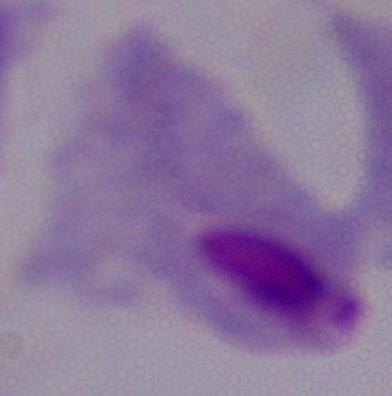
magnification = 1000x
modality = micrograph
identification = trichomonad